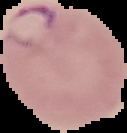

malaria_status: parasitized
preparation: thin blood film
image_size: 127×133 pixels
image_type: cell region segmented out of the field of view; surrounding area masked to black